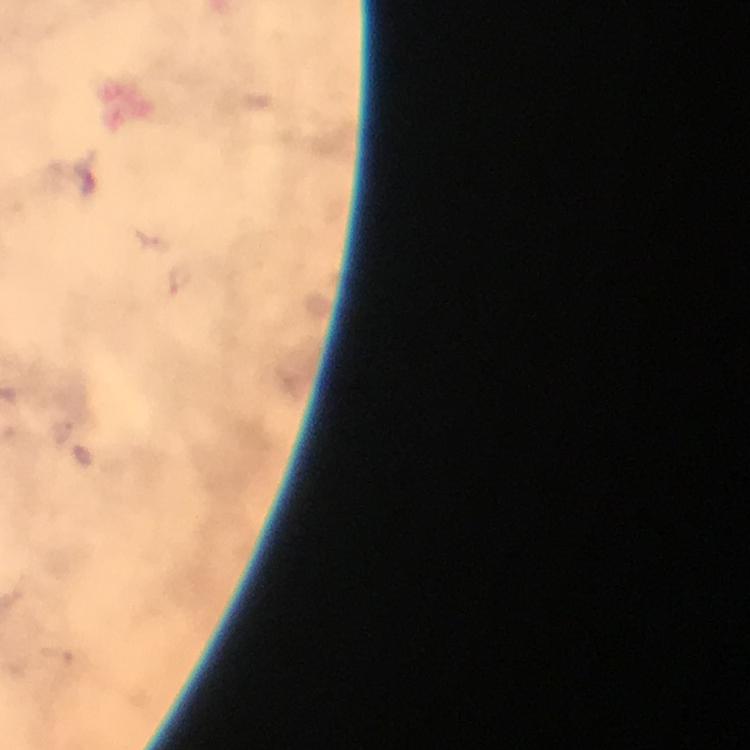
Approximate centers as (x, y) in pixels. Plasmodium parasite locations: (180, 282). From a diagnostic examination for malaria. Cropped region of a single field of view. Immersion oil applied. At 100x magnification. Giemsa-stained preparation. Image is 750×750 pixels. Smartphone photograph taken through a microscope. Thick blood film.